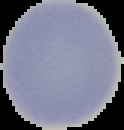

Segmented cell region on a black background. Malaria status: uninfected. From a thin blood smear. Image is 124×130 pixels.